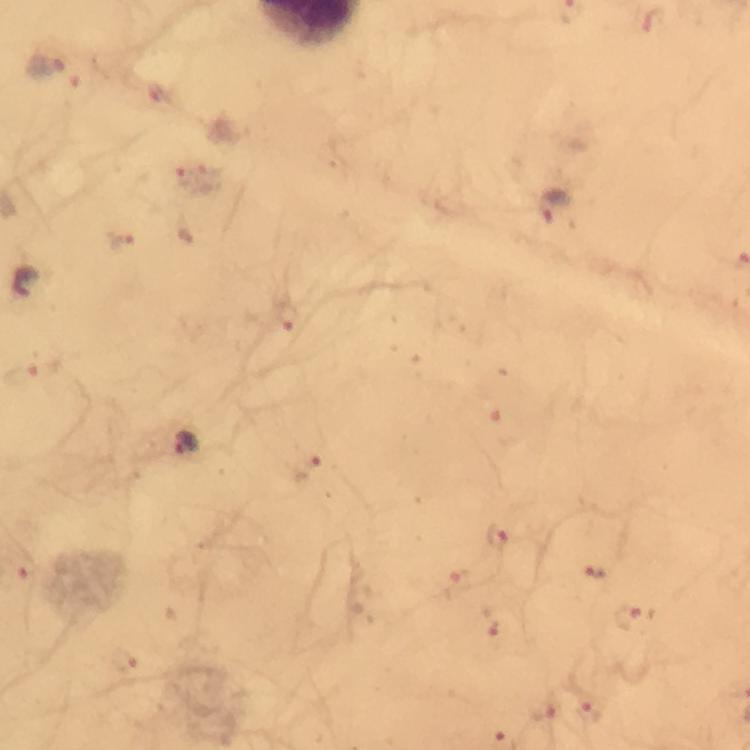

immersion oil = used
stain = Giemsa
image size = 750×750 pixels
cropped from = one field of view
preparation = thick smear
capture = smartphone mounted on the microscope
magnification = 100x
Plasmodium parasite locations = approximate centers as (x, y) in pixels: (47, 65), (211, 170), (181, 174), (556, 205), (126, 241), (28, 289), (285, 315), (508, 427), (191, 445), (307, 468), (499, 537), (596, 572), (456, 584), (629, 617), (492, 620), (125, 662), (544, 715), (592, 716)
context = from a malaria diagnostic workup